State the preparation type.
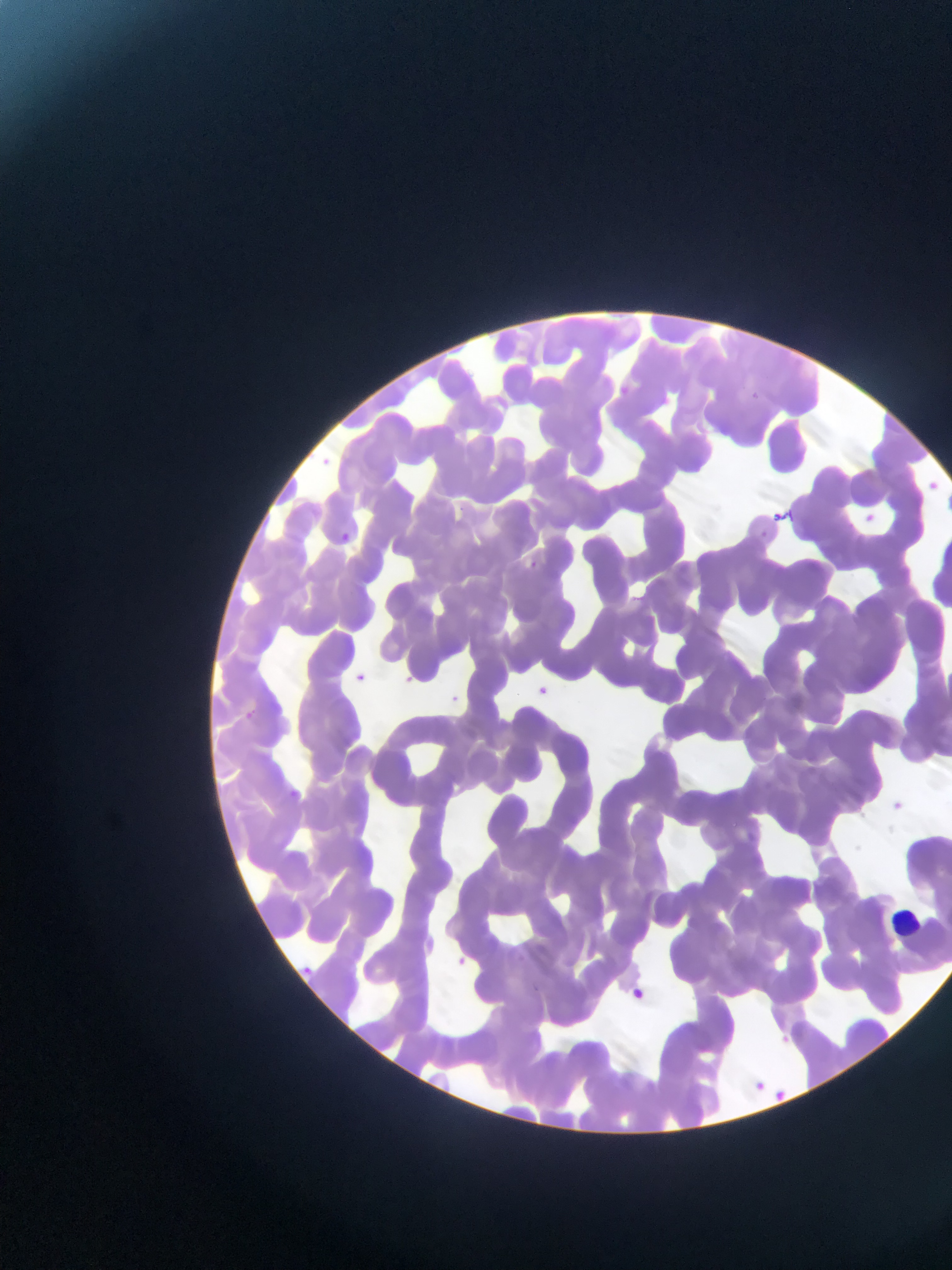

Thin blood film.

field of view = single
capture = mobile-phone photograph through a microscope
Plasmodium parasite locations = approximate bounding boxes as {left, top, right, bottom} in pixels: {616, 383, 634, 400}, {313, 454, 333, 472}, {921, 477, 941, 496}, {455, 502, 470, 517}, {768, 508, 788, 526}, {858, 509, 878, 527}, {334, 530, 353, 546}, {527, 560, 539, 571}, {524, 562, 541, 576}, {352, 671, 368, 686}, {348, 674, 373, 691}, {534, 683, 551, 698}, {446, 692, 462, 707}, {286, 787, 300, 802}, {884, 797, 910, 819}, {451, 955, 467, 969}, {297, 963, 318, 982}, {623, 987, 648, 1009}, {748, 1076, 771, 1098}, {769, 1084, 794, 1108}
country = Ghana
leukocyte locations = approximate bounding boxes as {left, top, right, bottom} in pixels: {888, 893, 928, 954}
image size = 952×1270 pixels